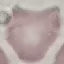
result = negative for malaria parasites
image type = cell patch, automatically extracted from a larger field of view and resized to 64 × 64 pixels
stain = Giemsa
capture = smartphone through the microscope eyepiece
preparation = thin blood film